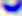

identification = Toxoplasma gondii
magnification = 400x
modality = photomicrograph